Identify the blood parasite species.
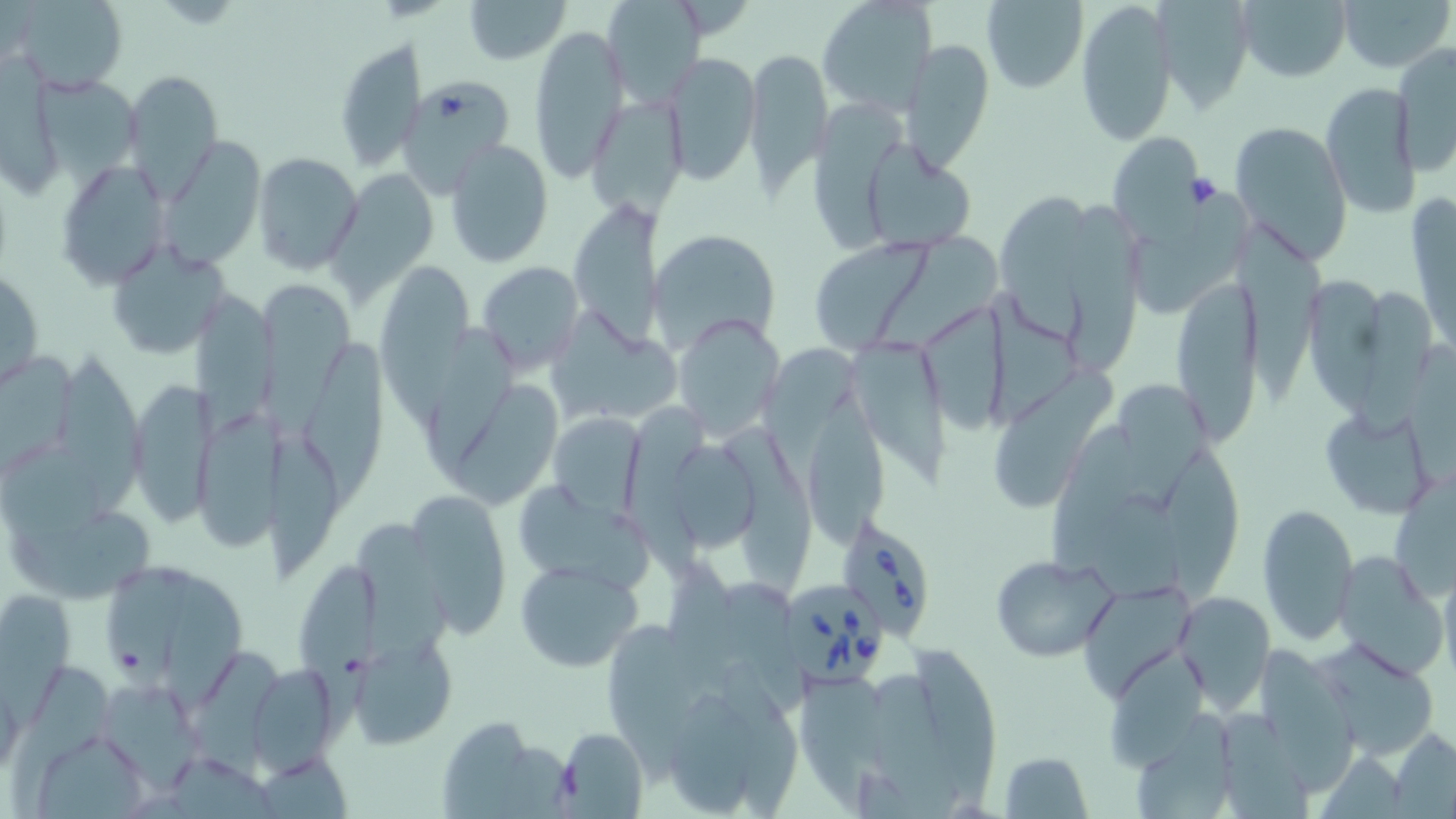
Babesia divergens.

Summary:
  - Coordinate format: approximate bounding boxes as (x1, y1, x2, y2) in pixels
  - Babesia divergens-infected red blood cell locations: (836, 513, 941, 640), (788, 577, 888, 690)
  - Uninfected red blood cell locations: (8, 0, 129, 93), (463, 0, 571, 65), (602, 0, 708, 108), (816, 0, 937, 114), (1075, 0, 1178, 147), (1157, 0, 1253, 116), (1235, 0, 1354, 83), (1338, 0, 1452, 75), (979, 1, 1089, 92), (529, 25, 629, 182), (334, 36, 424, 172), (902, 38, 995, 173), (1392, 43, 1456, 175), (745, 48, 830, 191), (663, 53, 760, 185), (2, 56, 69, 197), (122, 70, 222, 193), (38, 74, 143, 199), (399, 78, 514, 186), (1320, 81, 1420, 218), (587, 96, 687, 220), (806, 101, 919, 252), (1227, 121, 1352, 263), (1105, 129, 1204, 234), (444, 138, 554, 267), (164, 142, 266, 271), (860, 143, 976, 253), (252, 152, 363, 274), (57, 160, 169, 287), (325, 171, 440, 316), (999, 190, 1098, 347), (1139, 194, 1251, 315), (1063, 197, 1147, 376), (1410, 197, 1455, 356), (568, 199, 664, 347), (1232, 208, 1330, 408), (650, 227, 777, 349), (877, 231, 1008, 357), (104, 238, 231, 360), (807, 240, 927, 351), (477, 261, 584, 376), (372, 264, 475, 438), (1, 266, 44, 392), (1169, 274, 1259, 449), (1300, 275, 1382, 420), (257, 283, 359, 441), (1353, 283, 1431, 432), (989, 285, 1080, 431), (197, 293, 277, 434), (920, 302, 1016, 439), (543, 306, 685, 428), (671, 313, 786, 442), (425, 326, 518, 483), (850, 339, 955, 494), (300, 341, 391, 510), (761, 341, 868, 488), (0, 344, 80, 477), (58, 350, 154, 518), (994, 359, 1119, 518), (1117, 378, 1213, 508), (132, 379, 220, 529), (450, 381, 561, 513), (806, 393, 885, 547), (624, 402, 710, 577), (1319, 404, 1439, 522), (194, 410, 281, 554), (549, 413, 646, 516), (722, 422, 816, 601), (1050, 422, 1139, 581), (262, 441, 343, 574), (673, 442, 757, 556), (1154, 445, 1247, 602), (1394, 475, 1456, 603), (516, 485, 656, 594), (1085, 487, 1183, 604), (406, 492, 514, 635), (1256, 502, 1359, 645), (8, 511, 155, 609), (357, 515, 452, 681), (295, 551, 386, 754), (1335, 551, 1447, 676), (990, 554, 1117, 662), (106, 558, 190, 699), (515, 558, 642, 671), (667, 563, 740, 691), (1439, 565, 1456, 681), (159, 574, 249, 710), (719, 578, 814, 712), (1084, 582, 1199, 696), (0, 589, 72, 736), (1174, 589, 1274, 711), (605, 620, 687, 787), (1099, 634, 1211, 775), (351, 635, 457, 749), (1312, 639, 1440, 761), (911, 643, 996, 811), (1255, 643, 1359, 795), (196, 645, 283, 780), (720, 657, 801, 819), (8, 666, 114, 817), (256, 666, 340, 775), (797, 673, 913, 813), (872, 673, 972, 819), (104, 681, 203, 795), (671, 690, 757, 815), (1136, 707, 1234, 819), (1222, 711, 1314, 819), (436, 716, 553, 816), (555, 727, 648, 817), (1389, 730, 1456, 817), (41, 732, 155, 819), (997, 751, 1093, 818), (1317, 752, 1411, 819), (251, 753, 355, 815)
  - Modality: optical microscopy
  - Preparation: thin blood smear
  - Magnification: 1000x
  - Image size: 1456×819 pixels
  - Stain: May-Grünwald-Giemsa
  - Field of view: one of a larger specimen